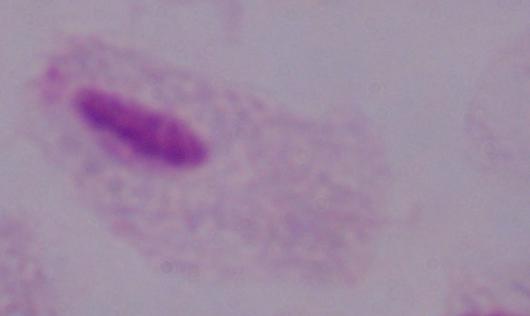
Summary:
  - Identification: trichomonad
  - Magnification: 1000x
  - Modality: micrograph